Look for parasitized red blood cells.
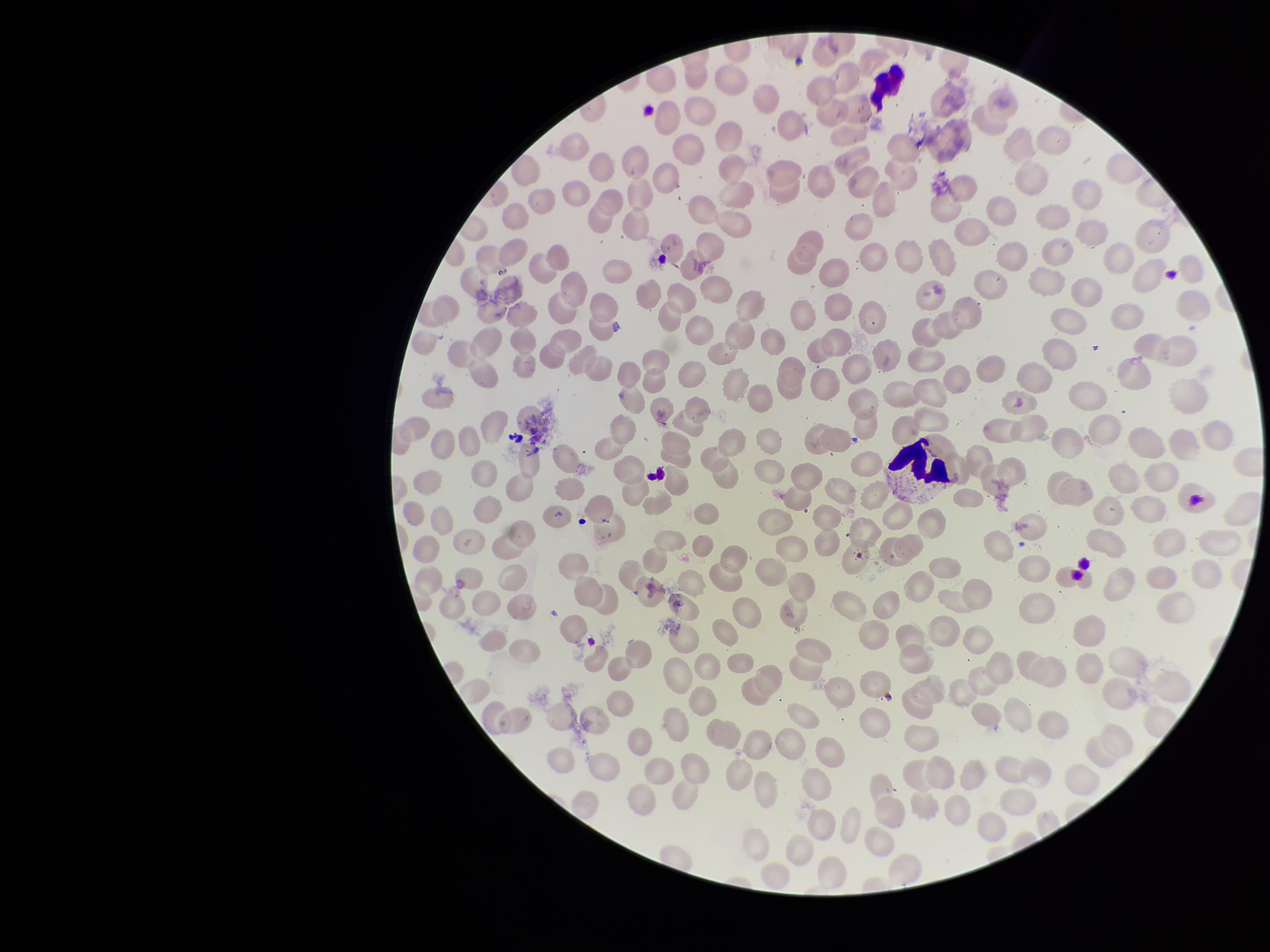
None identified.

Preparation: thin. Image is 1270×952 pixels. Photographed through the microscope eyepiece with a smartphone camera. Parasitized red blood cell count: 0. Red blood cell count: 254. Species reported for this patient: Plasmodium vivax. Single field of view. Stained with Giemsa. Patient malaria status: infected.